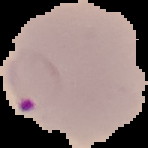
Summary:
  - Image type: cell region segmented out of the field of view; surrounding area masked to black
  - Image size: 148×148 pixels
  - Preparation: thin blood smear
  - Malaria status: parasitized